Identify the parasite.
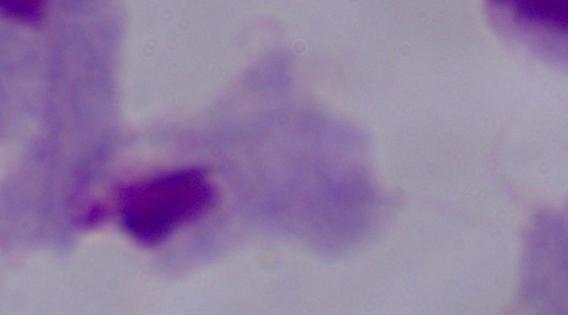

This is a trichomonad.

Summary:
  - Magnification: 1000x
  - Modality: micrograph